Locate every Trypanosoma brucei.
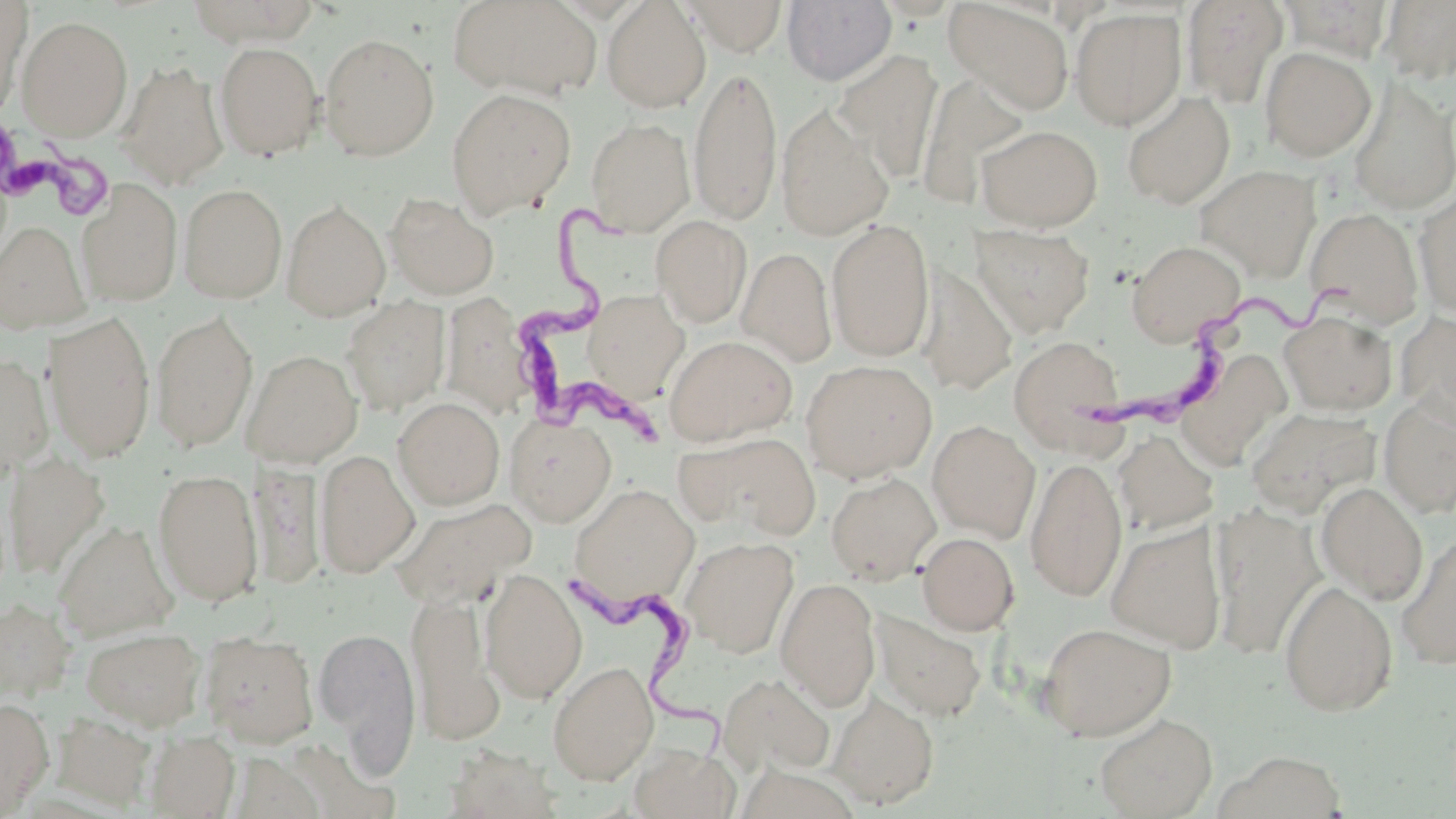
Approximate bounding boxes as (x1,y1)-(x2,y2) corner pairs in pixels.
Trypanosoma brucei: (1,114)-(123,225), (508,204)-(674,447), (1085,263)-(1367,438), (564,561)-(733,774).

Summary:
  - Uninfected red blood cell locations: (185,0)-(320,46), (448,0)-(602,102), (602,0)-(711,112), (681,0)-(788,56), (782,0)-(896,85), (944,0)-(1075,116), (1381,0)-(1456,85), (0,1)-(31,118), (1183,1)-(1288,108), (1278,1)-(1394,61), (1069,7)-(1186,131), (16,15)-(133,141), (319,33)-(439,161), (214,42)-(325,160), (1259,46)-(1376,162), (832,49)-(944,183), (117,62)-(230,189), (689,63)-(782,227), (920,74)-(1032,206), (1349,79)-(1456,215), (446,88)-(576,218), (1122,90)-(1236,209), (775,106)-(894,241), (586,117)-(695,236), (976,124)-(1102,231), (1195,164)-(1321,283), (76,177)-(183,306), (179,183)-(287,303), (1414,189)-(1456,319), (384,193)-(499,300), (282,199)-(390,321), (1305,207)-(1425,328), (651,215)-(752,327), (826,218)-(935,362), (0,220)-(92,335), (968,223)-(1095,337), (1126,240)-(1246,345), (738,247)-(837,367), (916,265)-(1018,395), (583,290)-(689,400), (440,292)-(535,419), (342,296)-(450,414), (151,309)-(258,451), (43,311)-(156,463), (1279,311)-(1397,414), (1396,311)-(1456,429), (664,335)-(797,446), (1008,335)-(1126,456), (243,349)-(363,466), (0,354)-(54,476), (801,359)-(938,482), (393,397)-(505,510), (1378,397)-(1456,518), (1246,406)-(1385,515), (506,415)-(617,526), (927,420)-(1041,542), (1113,430)-(1218,536), (675,431)-(820,540), (315,449)-(420,578), (3,451)-(109,579), (1025,456)-(1127,602), (153,468)-(264,606), (826,472)-(941,584), (1315,482)-(1429,605), (568,483)-(699,610), (390,496)-(536,608), (1213,509)-(1322,660), (53,520)-(179,641), (1105,521)-(1227,653), (917,532)-(1019,635), (1396,532)-(1456,670), (681,537)-(798,657), (480,568)-(587,704), (775,577)-(881,711), (1280,580)-(1398,717), (407,590)-(505,746), (1,599)-(75,701), (872,609)-(987,722), (1037,621)-(1177,741), (313,624)-(421,772), (81,627)-(206,731), (200,633)-(319,747), (548,661)-(659,785), (717,672)-(835,776), (829,690)-(938,809), (0,697)-(53,816), (53,712)-(158,810), (1094,712)-(1217,818), (145,730)-(240,818), (630,743)-(739,819), (1212,750)-(1348,819)
  - Slide-level diagnosis: Trypanosoma brucei
  - Field of view: one of a larger specimen
  - Magnification: 1000x
  - Stain: May-Grünwald-Giemsa
  - Modality: light microscopy
  - Image size: 1456×819 pixels
  - Preparation: thin blood film